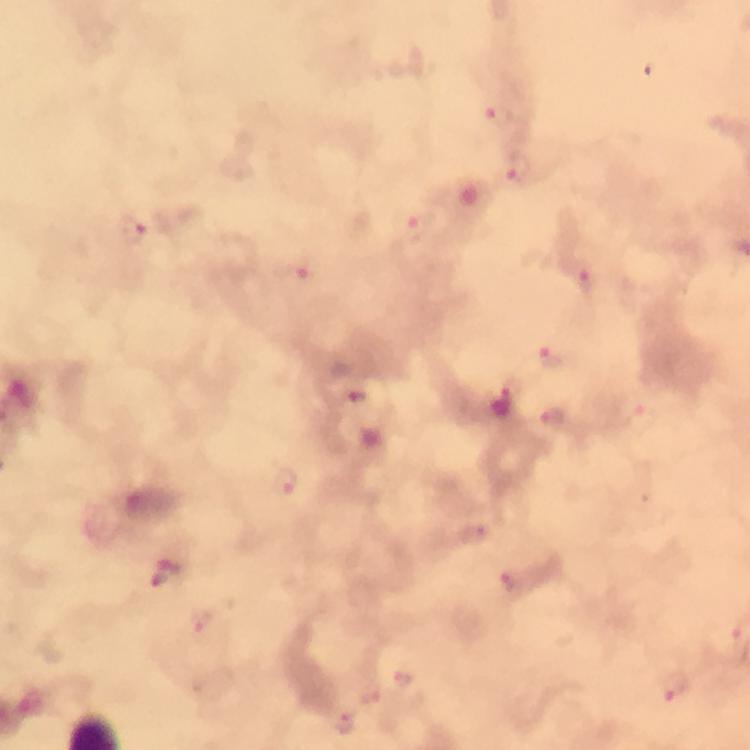
Approximate centers as {x, y} in pixels. Plasmodium parasite locations: {500, 117}, {518, 169}, {132, 229}, {417, 229}, {296, 276}, {589, 281}, {550, 356}, {358, 396}, {507, 400}, {553, 417}, {284, 482}, {479, 533}, {166, 573}, {511, 582}, {204, 621}, {403, 684}, {673, 689}, {343, 722}. From a malaria diagnostic workup. 100x magnification. Smartphone photograph taken through a microscope. Image is 750×750 pixels. Cropped region of a single field of view. Thick smear. Immersion oil applied. Giemsa stain.